Assess the morphology of the erythrocytes.
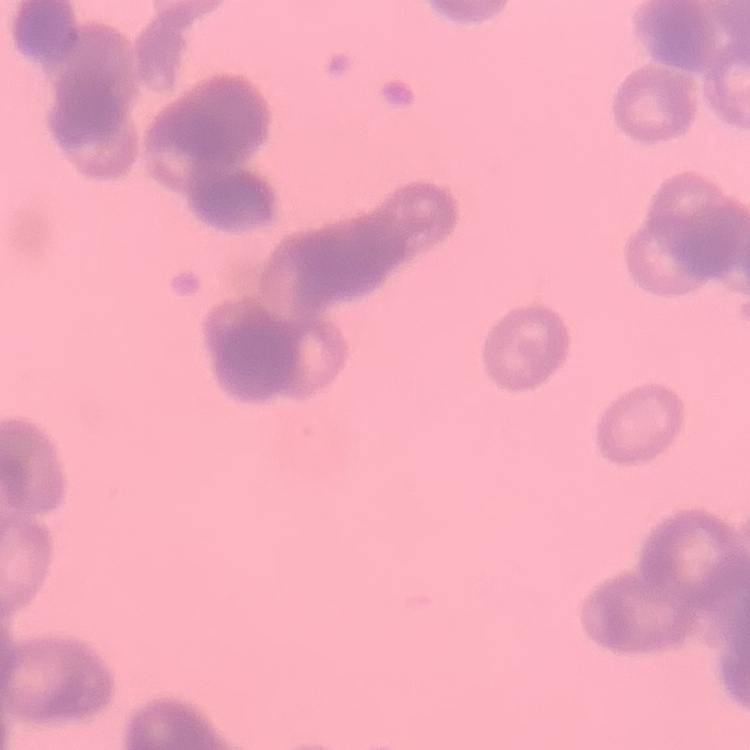

Rouleaux formation.

preparation = thin peripheral smear
image type = square crop of a larger photomicrograph
stain = Field's or Giemsa